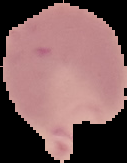
Summary:
  - Malaria status: parasitized
  - Image size: 127×163 pixels
  - Image type: segmented cell region with the area outside set to black
  - Preparation: thin blood film